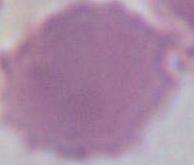
identification: red blood cell
magnification: 1000x
modality: photomicrograph